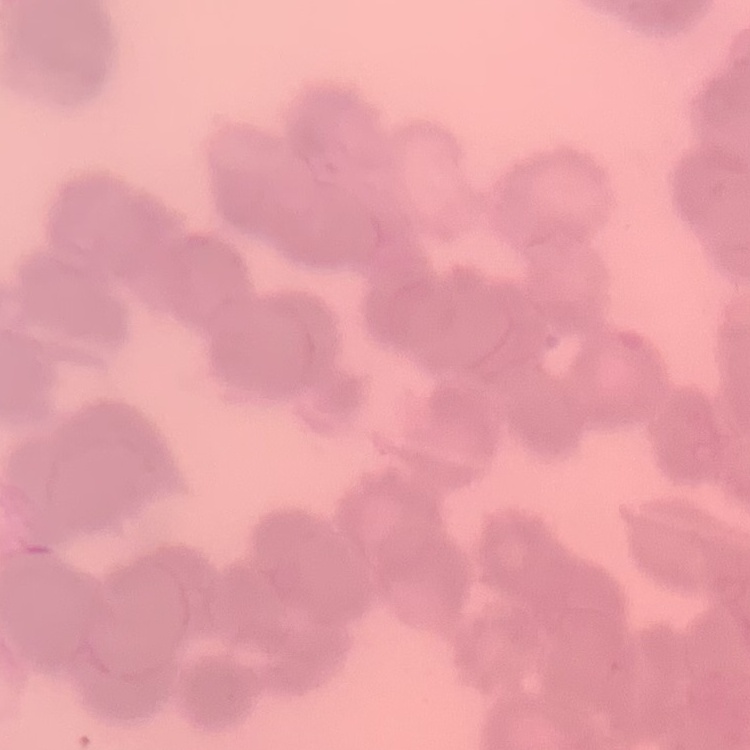
red blood cell morphology = rouleaux formation
stain = Field's or Giemsa
preparation = thin blood smear
image type = square crop of a larger photomicrograph